Outline platelets.
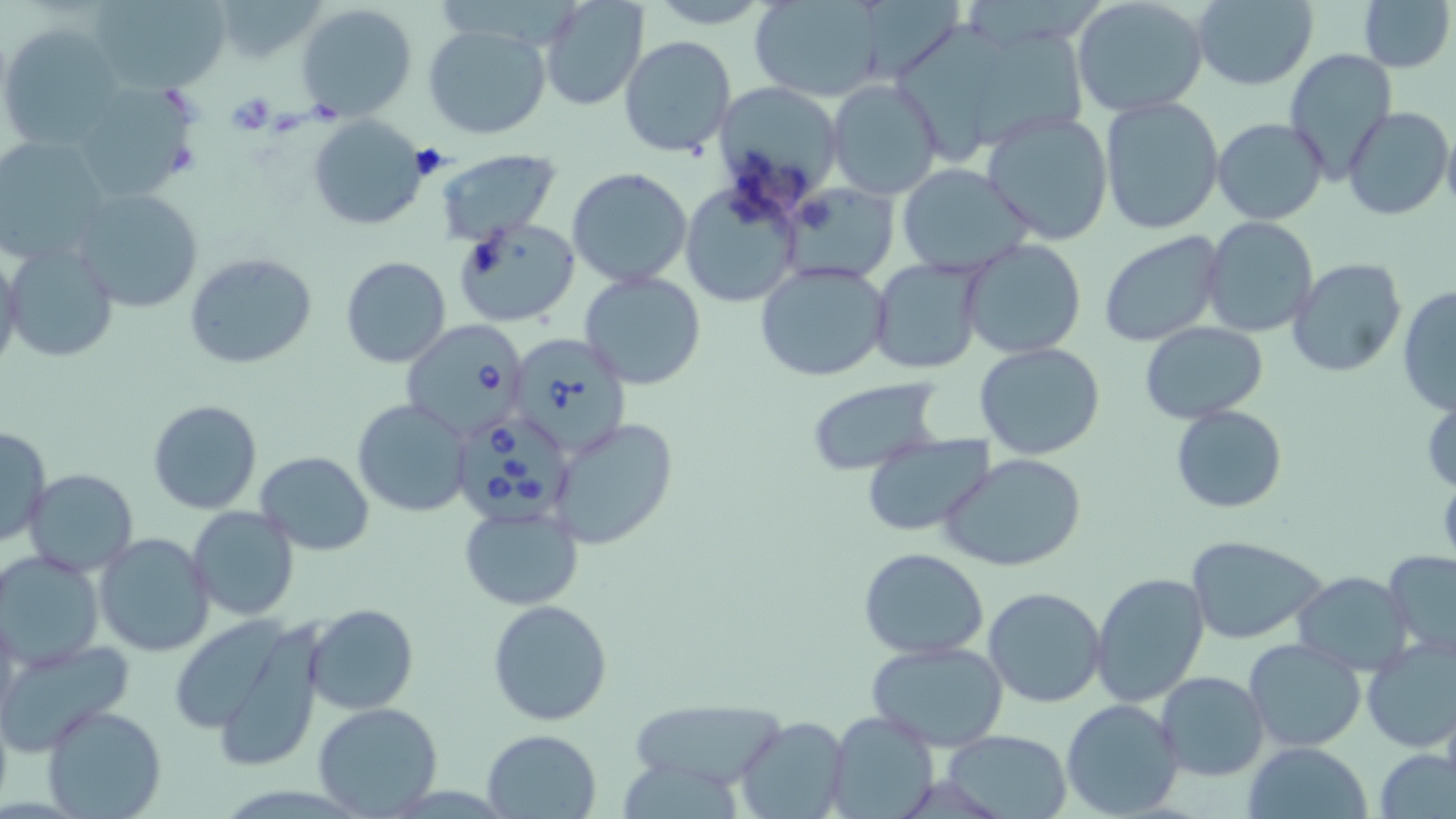
Approximate bounding boxes as named x1/y1/x2/y2 corners in pixels.
Platelets: (x1=226, y1=90, x2=275, y2=135), (x1=305, y1=99, x2=344, y2=124).

Summary:
  - Uninfected red blood cell locations: (x1=86, y1=0, x2=231, y2=94), (x1=212, y1=0, x2=329, y2=64), (x1=644, y1=0, x2=775, y2=29), (x1=1070, y1=0, x2=1210, y2=118), (x1=1189, y1=0, x2=1319, y2=90), (x1=1358, y1=0, x2=1454, y2=73), (x1=749, y1=1, x2=884, y2=101), (x1=542, y1=2, x2=647, y2=110), (x1=297, y1=4, x2=418, y2=117), (x1=3, y1=25, x2=125, y2=150), (x1=423, y1=25, x2=552, y2=140), (x1=620, y1=36, x2=735, y2=157), (x1=1284, y1=49, x2=1396, y2=180), (x1=827, y1=78, x2=942, y2=201), (x1=68, y1=81, x2=197, y2=202), (x1=712, y1=83, x2=845, y2=208), (x1=1097, y1=96, x2=1224, y2=235), (x1=1342, y1=105, x2=1452, y2=221), (x1=982, y1=112, x2=1114, y2=245), (x1=308, y1=114, x2=430, y2=231), (x1=1212, y1=117, x2=1328, y2=224), (x1=1441, y1=122, x2=1456, y2=216), (x1=0, y1=137, x2=114, y2=267), (x1=433, y1=147, x2=562, y2=243), (x1=898, y1=163, x2=1033, y2=275), (x1=566, y1=166, x2=694, y2=288), (x1=784, y1=182, x2=897, y2=286), (x1=680, y1=183, x2=801, y2=306), (x1=69, y1=188, x2=204, y2=314), (x1=453, y1=215, x2=579, y2=327), (x1=1202, y1=218, x2=1318, y2=338), (x1=1099, y1=232, x2=1224, y2=349), (x1=961, y1=238, x2=1088, y2=358), (x1=4, y1=242, x2=117, y2=363), (x1=0, y1=248, x2=25, y2=380), (x1=183, y1=252, x2=317, y2=368), (x1=340, y1=256, x2=451, y2=369), (x1=1286, y1=257, x2=1407, y2=378), (x1=868, y1=258, x2=984, y2=375), (x1=754, y1=259, x2=893, y2=383), (x1=578, y1=271, x2=708, y2=390), (x1=1397, y1=285, x2=1456, y2=416), (x1=1139, y1=322, x2=1266, y2=422), (x1=975, y1=342, x2=1107, y2=461), (x1=805, y1=377, x2=946, y2=476), (x1=352, y1=398, x2=472, y2=517), (x1=146, y1=399, x2=265, y2=515), (x1=1170, y1=404, x2=1287, y2=514), (x1=548, y1=417, x2=679, y2=553), (x1=0, y1=426, x2=49, y2=547), (x1=862, y1=433, x2=995, y2=536), (x1=255, y1=452, x2=374, y2=556), (x1=940, y1=454, x2=1087, y2=573), (x1=23, y1=469, x2=140, y2=576), (x1=459, y1=505, x2=583, y2=610), (x1=188, y1=506, x2=299, y2=621), (x1=94, y1=531, x2=216, y2=659), (x1=1186, y1=536, x2=1326, y2=644), (x1=858, y1=548, x2=989, y2=660), (x1=1383, y1=548, x2=1456, y2=659), (x1=0, y1=551, x2=107, y2=670), (x1=1293, y1=570, x2=1414, y2=672), (x1=1091, y1=572, x2=1212, y2=709), (x1=983, y1=586, x2=1107, y2=709), (x1=487, y1=598, x2=613, y2=726), (x1=304, y1=604, x2=418, y2=714), (x1=1, y1=609, x2=23, y2=733), (x1=177, y1=614, x2=330, y2=764), (x1=1361, y1=637, x2=1455, y2=754), (x1=0, y1=638, x2=132, y2=755), (x1=1243, y1=639, x2=1366, y2=752), (x1=866, y1=641, x2=1009, y2=750), (x1=1155, y1=668, x2=1270, y2=781), (x1=628, y1=699, x2=789, y2=793), (x1=1060, y1=699, x2=1184, y2=819), (x1=313, y1=702, x2=443, y2=815), (x1=41, y1=704, x2=167, y2=819), (x1=824, y1=710, x2=939, y2=819), (x1=733, y1=716, x2=849, y2=819), (x1=482, y1=730, x2=602, y2=818), (x1=942, y1=730, x2=1074, y2=819), (x1=1242, y1=742, x2=1372, y2=819), (x1=1377, y1=749, x2=1455, y2=819)
  - Babesia divergens-infected red blood cell locations: (x1=401, y1=320, x2=530, y2=439), (x1=506, y1=335, x2=631, y2=458), (x1=458, y1=414, x2=567, y2=525)
  - Slide-level diagnosis: Babesia divergens
  - Modality: optical microscopy
  - Image size: 1456×819 pixels
  - Field of view: one of a larger specimen
  - Preparation: thin blood smear
  - Stain: May-Grünwald-Giemsa
  - Magnification: 1000x